Name the parasite shown.
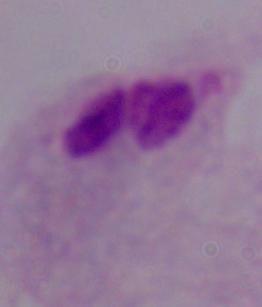

This is a trichomonad.

Summary:
  - Magnification: 1000x
  - Modality: photomicrograph